Name the parasite shown.
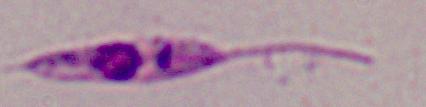

This is Leishmania.

Summary:
  - Modality: micrograph
  - Magnification: 1000x